Assess this cell for malaria.
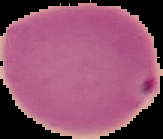
Parasitized.

image_size: 163×139 pixels
preparation: thin blood smear
image_type: segmented cell region on a black background